Report the malaria status of this cell.
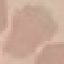

It is uninfected.

Summary:
  - Image type: automatically extracted cell patch, resized to 64 × 64 pixels
  - Capture: smartphone through the microscope eyepiece
  - Stain: Giemsa
  - Preparation: thin smear